Outline malaria parasites and classify them by life-cycle stage.
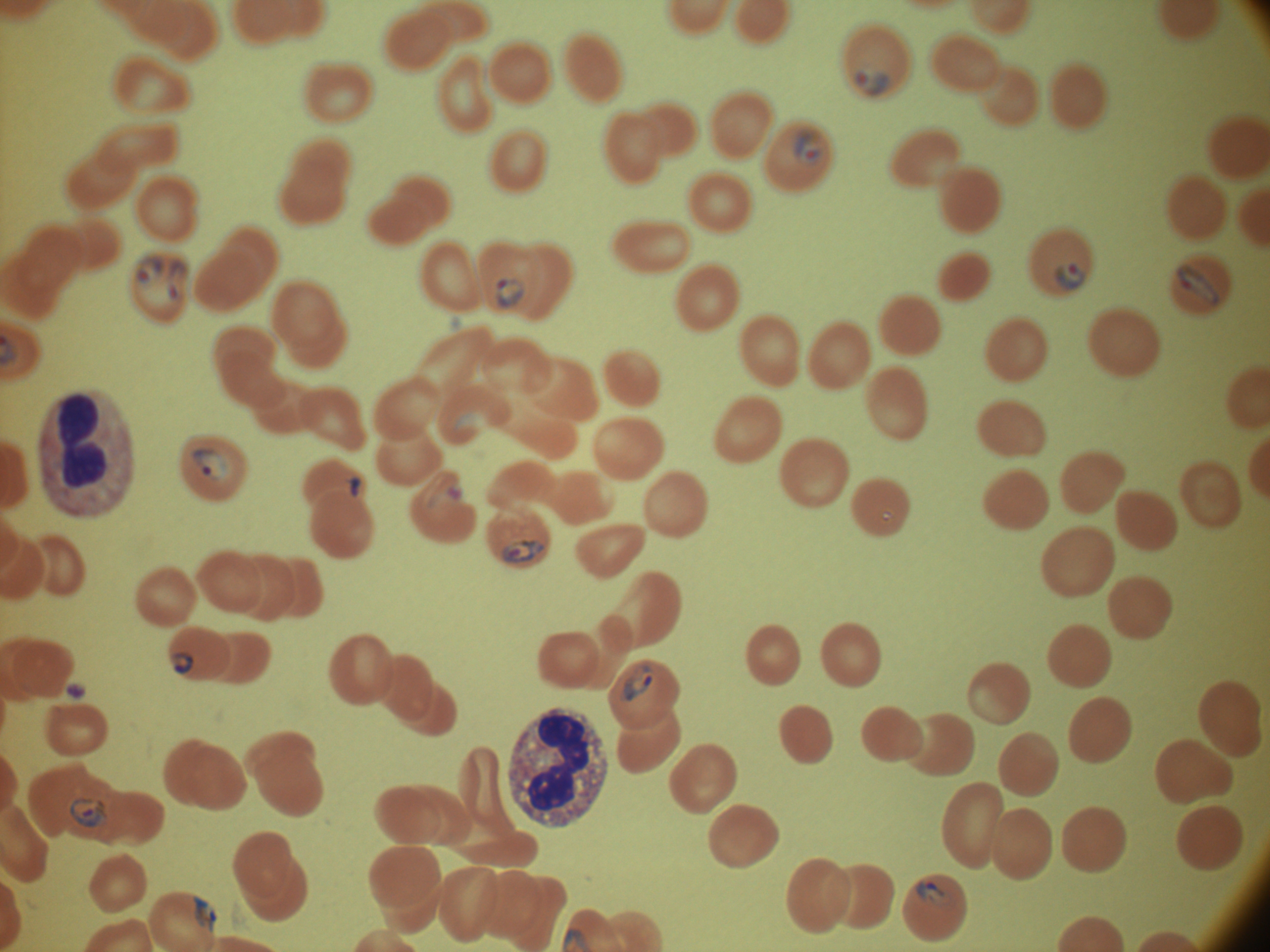
Approximate bounding boxes as (x1, y1, x2, y2) in pixels, from the source annotation, which is not necessarily exhaustive.
Ring forms: (855, 71, 888, 96), (794, 130, 822, 164), (135, 257, 165, 284), (167, 260, 187, 280), (1055, 262, 1086, 291), (1176, 263, 1219, 306), (496, 278, 525, 308), (168, 282, 179, 300), (193, 449, 228, 481), (349, 477, 362, 497), (880, 510, 895, 523), (504, 541, 545, 562), (173, 653, 194, 674), (622, 665, 653, 701), (70, 798, 107, 828), (916, 881, 950, 906), (193, 896, 218, 932).

Summary:
  - Image size: 1270×952 pixels
  - Magnification: 100x
  - Microscope: Leica DM2000 with built-in camera
  - Preparation: thin blood film
  - Species: Plasmodium falciparum
  - Stain: Giemsa
  - Field of view: one from this slide